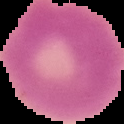
image_type: segmented cell region with the area outside set to black
malaria_status: uninfected
image_size: 124×124 pixels
preparation: thin blood smear